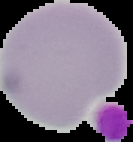

image size = 133×142 pixels
result = no malaria parasites seen
image type = segmented cell region on a black background
preparation = thin blood film